Locate every blood parasite and identify its species.
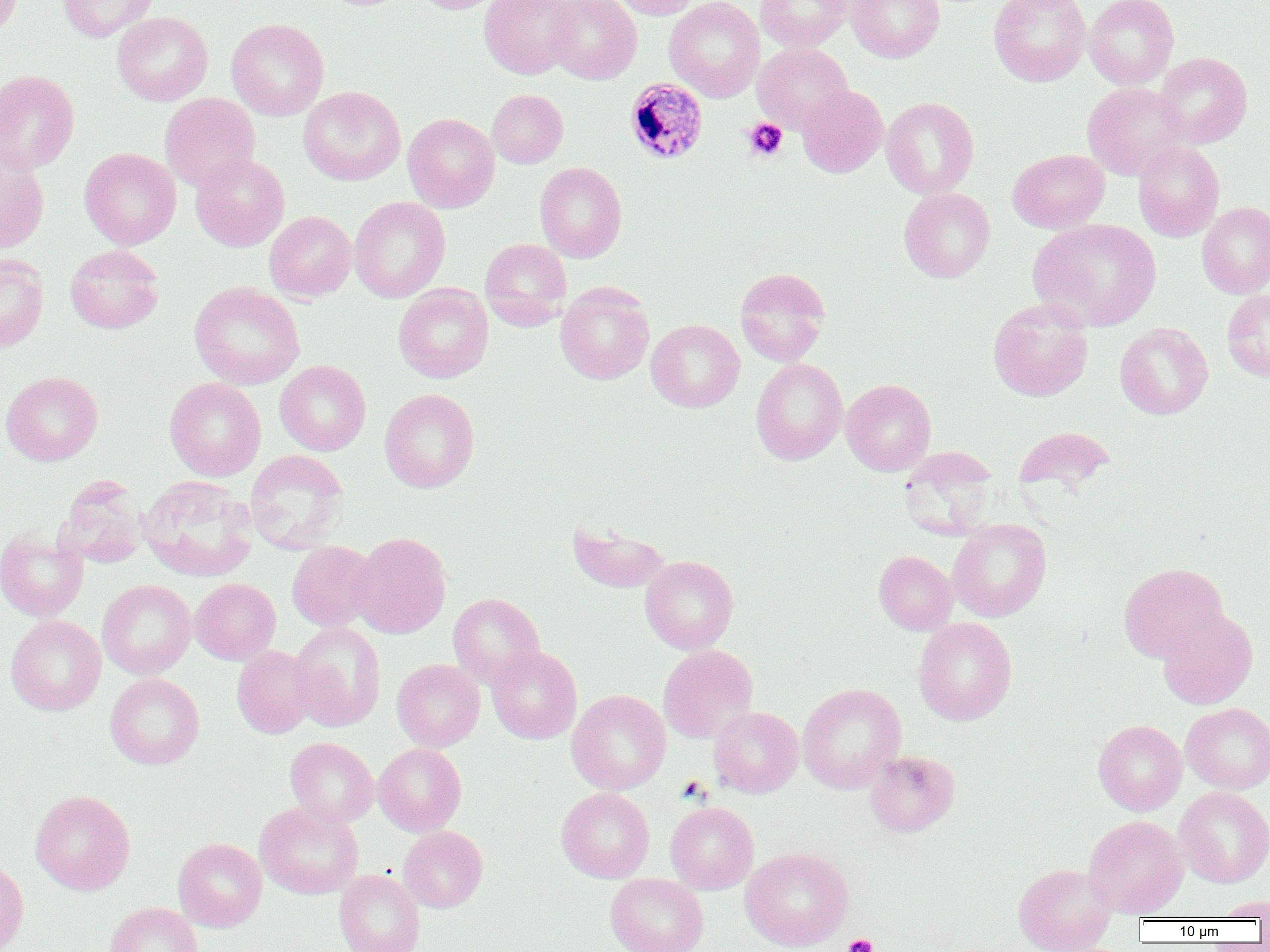

Approximate bounding boxes as (x1,y1)-(x2,y2) corner pairs in pixels.
Plasmodium malariae-infected red blood cells: (625,78)-(708,165).
No Plasmodium falciparum, Plasmodium ovale, Plasmodium vivax, Babesia divergens, or Trypanosoma brucei observed.

slide_level_diagnosis: Plasmodium malariae
preparation: thin blood film
magnification: 1000x
modality: optical microscopy
image_size: 1270×952 pixels
field_of_view: one of a larger specimen
platelet_locations: 'approximate bounding boxes as (x1,y1)-(x2,y2) corner pairs in pixels: (742,118)-(788,162), (843,934)-(878,952)'
uninfected_red_blood_cell_locations: 'approximate bounding boxes as (x1,y1)-(x2,y2) corner pairs in pixels: (0,0)-(22,42), (57,0)-(159,42), (413,0)-(503,13), (479,0)-(580,79), (546,0)-(641,84), (610,0)-(701,19), (664,0)-(765,102), (755,0)-(852,51), (847,0)-(945,62), (989,0)-(1091,86), (1084,0)-(1179,89), (112,12)-(213,106), (226,18)-(329,121), (752,43)-(853,133), (1155,52)-(1253,148), (0,69)-(80,174), (1082,82)-(1190,180), (797,85)-(887,177), (298,86)-(406,186), (487,89)-(568,168), (159,93)-(260,191), (881,97)-(979,199), (402,113)-(500,213), (1133,141)-(1224,242), (79,147)-(181,249), (1008,149)-(1109,233), (0,151)-(49,253), (190,154)-(289,251), (535,161)-(627,262), (899,187)-(996,282), (349,197)-(450,303), (1197,201)-(1270,299), (264,211)-(357,302), (1029,218)-(1161,331), (480,238)-(572,331), (64,244)-(164,334), (0,255)-(49,353), (734,267)-(831,366), (189,281)-(305,389), (555,282)-(655,385), (393,283)-(493,383), (1221,289)-(1270,383), (988,298)-(1093,401), (646,319)-(744,412), (1114,322)-(1213,420), (750,357)-(848,465), (275,360)-(371,456), (1,371)-(103,466), (164,377)-(266,481), (841,379)-(936,475), (380,388)-(479,492), (1014,426)-(1115,494), (245,449)-(349,554), (138,475)-(258,581), (55,478)-(148,568), (947,519)-(1052,621), (567,521)-(671,593), (0,527)-(88,622), (352,532)-(452,639), (287,541)-(378,631), (873,550)-(958,635), (640,555)-(738,654), (1118,563)-(1228,662), (190,578)-(281,665), (97,579)-(196,680), (447,593)-(545,688), (1156,607)-(1258,709), (5,615)-(106,716), (913,617)-(1017,725), (289,621)-(386,732), (659,644)-(758,743), (232,645)-(317,738), (486,645)-(582,744), (391,659)-(485,751), (105,673)-(204,769), (797,683)-(906,793), (566,689)-(671,794), (1181,703)-(1270,794), (708,706)-(804,798), (1093,719)-(1187,815), (285,737)-(379,827), (373,743)-(466,836), (865,750)-(960,837), (1174,786)-(1270,887), (556,787)-(654,882), (30,790)-(135,895), (255,801)-(363,899), (664,801)-(759,894), (1084,815)-(1188,917), (399,826)-(487,912), (173,837)-(267,931), (740,846)-(853,951), (0,860)-(29,952), (1013,862)-(1117,952), (334,869)-(425,952), (605,873)-(709,952), (1211,896)-(1270,920), (105,902)-(202,952)'